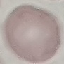
Summary:
  - Malaria status: uninfected
  - Image type: automatically extracted cell patch, resized to 64 × 64 pixels
  - Stain: Giemsa
  - Capture: smartphone camera at the microscope eyepiece
  - Preparation: thin blood smear